Outline each uninfected red blood cell.
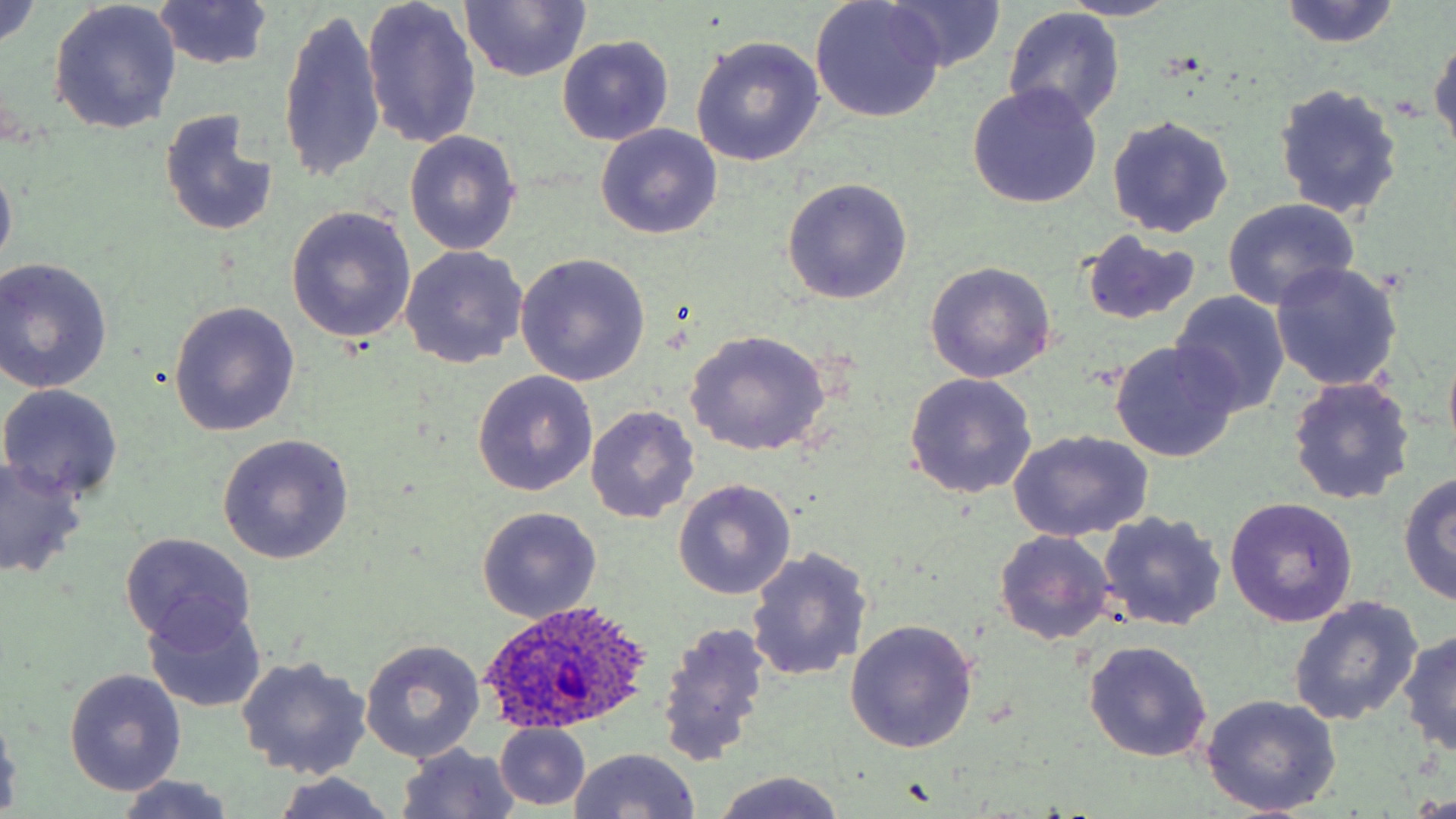
Approximate bounding boxes as (x1, y1, x2, y2) in pixels.
Uninfected red blood cells: (362, 0, 482, 150), (877, 0, 1008, 74), (1057, 0, 1185, 22), (0, 1, 43, 52), (1280, 1, 1401, 49), (459, 2, 590, 83), (810, 2, 945, 122), (49, 3, 182, 135), (151, 3, 276, 71), (277, 6, 385, 187), (1003, 8, 1126, 126), (1429, 30, 1456, 156), (557, 35, 674, 146), (689, 37, 825, 168), (1273, 83, 1404, 220), (967, 85, 1100, 208), (160, 109, 280, 240), (1107, 115, 1234, 238), (596, 124, 722, 239), (404, 130, 522, 256), (0, 156, 17, 276), (781, 178, 913, 303), (1221, 198, 1361, 310), (287, 206, 419, 344), (1079, 231, 1202, 326), (399, 246, 528, 368), (515, 254, 653, 386), (0, 258, 113, 393), (1270, 262, 1402, 393), (924, 264, 1056, 384), (1170, 291, 1290, 417), (167, 301, 301, 436), (683, 331, 831, 457), (1109, 341, 1240, 464), (1441, 342, 1456, 459), (472, 371, 597, 496), (903, 374, 1037, 499), (1286, 377, 1415, 506), (0, 384, 124, 503), (585, 405, 699, 523), (1008, 430, 1154, 542), (218, 434, 354, 564), (0, 456, 89, 579), (1049, 457, 1194, 599), (1396, 473, 1456, 605), (673, 481, 796, 601), (1225, 497, 1357, 628), (476, 507, 602, 623), (1097, 510, 1227, 632), (994, 530, 1116, 646), (119, 533, 255, 648), (747, 547, 871, 683), (1288, 597, 1423, 727), (144, 603, 268, 713), (656, 620, 771, 767), (845, 620, 979, 754), (1397, 629, 1456, 757), (360, 638, 486, 763), (1083, 640, 1212, 762), (235, 656, 372, 779), (65, 669, 187, 795), (1200, 694, 1341, 815), (0, 708, 23, 814), (495, 724, 590, 810), (396, 744, 522, 819), (568, 748, 702, 819), (712, 772, 846, 819), (270, 773, 398, 819), (113, 776, 242, 817).

Summary:
  - Plasmodium ovale-infected red blood cell locations: (480, 602, 657, 734)
  - Slide-level diagnosis: Plasmodium ovale
  - Field of view: single
  - Preparation: thin blood smear
  - Magnification: 1000x
  - Modality: light microscopy
  - Stain: May-Grünwald-Giemsa
  - Image size: 1456×819 pixels